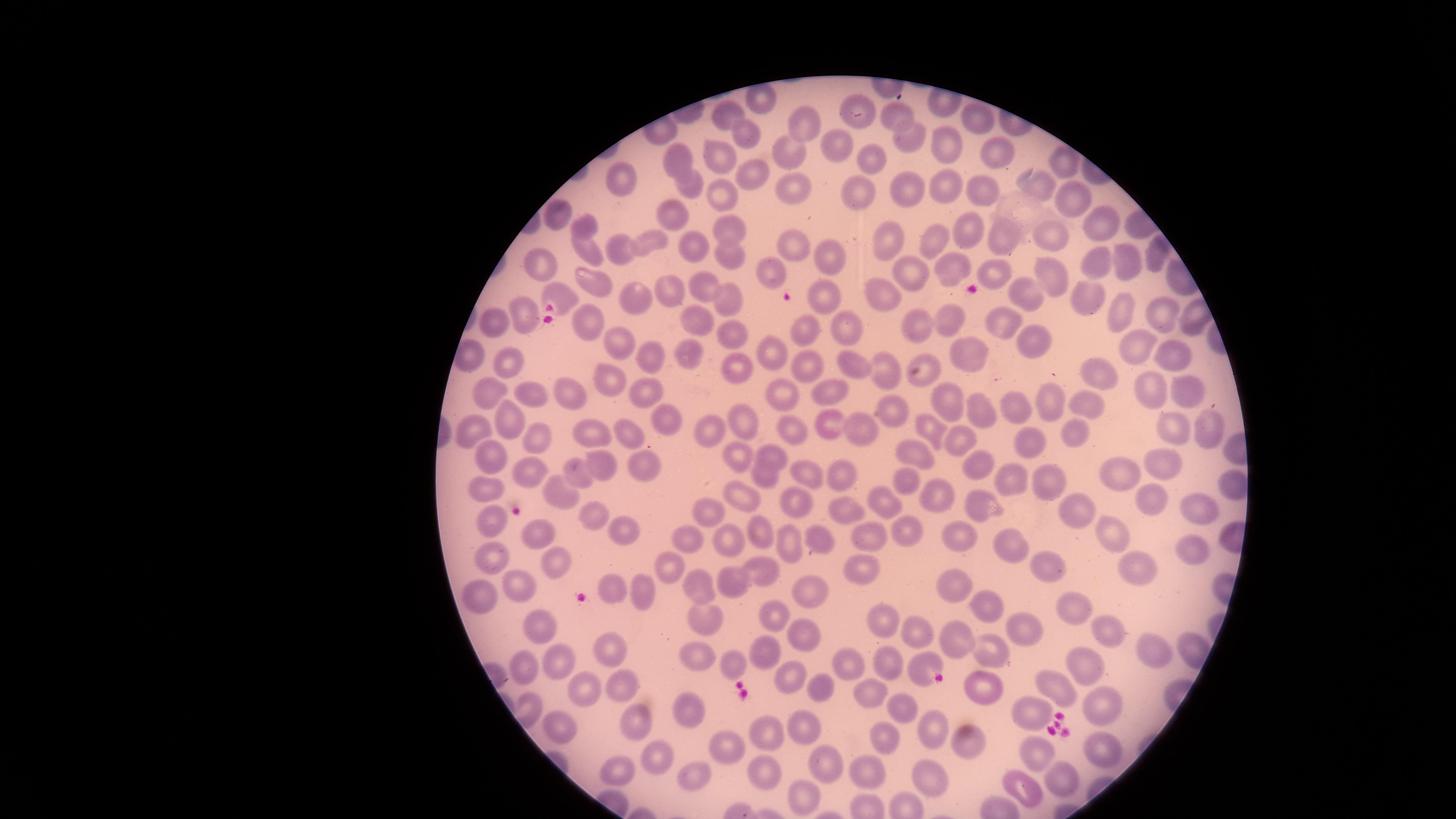

Approximate marker points, in pixels from the top-left corner. Uninfected red blood cells: (x=758, y=105), (x=858, y=106), (x=723, y=113), (x=896, y=117), (x=976, y=118), (x=800, y=123), (x=745, y=132), (x=909, y=141), (x=787, y=148), (x=840, y=149), (x=947, y=150), (x=673, y=152), (x=718, y=153), (x=991, y=153), (x=873, y=155), (x=1058, y=164), (x=619, y=177), (x=752, y=177), (x=687, y=183), (x=795, y=184), (x=949, y=187), (x=1039, y=187), (x=904, y=188), (x=717, y=190), (x=860, y=192), (x=985, y=193), (x=1070, y=201), (x=560, y=216), (x=673, y=217), (x=584, y=225), (x=1100, y=225), (x=724, y=226), (x=963, y=231), (x=1046, y=237), (x=647, y=241), (x=893, y=241), (x=933, y=241), (x=1004, y=241), (x=793, y=242), (x=583, y=244), (x=621, y=244), (x=693, y=248), (x=724, y=256), (x=833, y=258), (x=1094, y=259), (x=1122, y=260), (x=545, y=261), (x=953, y=267), (x=770, y=270), (x=998, y=273), (x=1047, y=273), (x=907, y=275), (x=704, y=283), (x=589, y=284), (x=555, y=290), (x=877, y=291), (x=669, y=292), (x=819, y=292), (x=1020, y=292), (x=627, y=293), (x=727, y=296), (x=1083, y=297), (x=522, y=312), (x=1160, y=312), (x=1116, y=314), (x=998, y=316), (x=948, y=321), (x=591, y=323), (x=695, y=323), (x=917, y=325), (x=490, y=326), (x=841, y=327), (x=803, y=329), (x=730, y=330), (x=620, y=341), (x=1034, y=342), (x=1129, y=342), (x=463, y=351), (x=1182, y=353), (x=684, y=354), (x=773, y=354), (x=964, y=354), (x=653, y=356), (x=850, y=359), (x=803, y=365), (x=512, y=366), (x=730, y=368), (x=1096, y=369), (x=885, y=372), (x=924, y=372), (x=610, y=378), (x=830, y=388), (x=647, y=389), (x=1182, y=389), (x=533, y=391), (x=1155, y=391), (x=497, y=392), (x=781, y=392), (x=572, y=395), (x=1049, y=400), (x=944, y=402), (x=1084, y=403), (x=889, y=407), (x=1020, y=407), (x=982, y=410), (x=514, y=417), (x=739, y=419), (x=670, y=420), (x=829, y=423), (x=1169, y=425), (x=1206, y=426), (x=864, y=428), (x=468, y=429), (x=626, y=429), (x=932, y=429), (x=715, y=432), (x=792, y=432), (x=586, y=433), (x=1068, y=433), (x=1026, y=438), (x=957, y=439), (x=536, y=441), (x=771, y=451), (x=912, y=453), (x=489, y=457), (x=739, y=457), (x=979, y=463), (x=648, y=464), (x=529, y=465), (x=604, y=465), (x=1156, y=465), (x=585, y=471), (x=838, y=471), (x=810, y=473), (x=1011, y=473), (x=1119, y=473), (x=764, y=477), (x=901, y=477), (x=1046, y=477), (x=1224, y=481), (x=564, y=491), (x=488, y=493), (x=744, y=494), (x=932, y=498), (x=1150, y=498), (x=798, y=503), (x=881, y=503), (x=970, y=505), (x=703, y=511), (x=843, y=511), (x=1193, y=511), (x=1080, y=512), (x=596, y=516), (x=493, y=517), (x=910, y=524), (x=626, y=528), (x=536, y=530), (x=768, y=530), (x=1108, y=530), (x=958, y=534), (x=863, y=535), (x=691, y=537), (x=795, y=538), (x=734, y=543), (x=815, y=543), (x=1007, y=546), (x=1190, y=554), (x=493, y=557), (x=757, y=565), (x=861, y=565), (x=673, y=567), (x=557, y=570), (x=1134, y=571), (x=1055, y=575), (x=738, y=579), (x=516, y=583), (x=695, y=583), (x=618, y=587), (x=960, y=587), (x=640, y=588), (x=807, y=588), (x=480, y=596), (x=985, y=606), (x=1083, y=609), (x=776, y=612), (x=880, y=615), (x=714, y=624), (x=545, y=628), (x=1028, y=630), (x=797, y=632), (x=909, y=632), (x=1114, y=632), (x=961, y=643), (x=1157, y=644), (x=611, y=645), (x=993, y=652), (x=698, y=655), (x=765, y=656), (x=557, y=663), (x=890, y=663), (x=921, y=664), (x=729, y=666), (x=527, y=667), (x=850, y=667), (x=1087, y=667), (x=790, y=675), (x=619, y=680), (x=1056, y=687), (x=586, y=689), (x=815, y=691), (x=984, y=691), (x=870, y=694), (x=1106, y=702), (x=896, y=706), (x=692, y=711), (x=1031, y=716), (x=638, y=719), (x=556, y=728), (x=807, y=729), (x=929, y=732), (x=886, y=735), (x=769, y=739), (x=968, y=743), (x=724, y=747), (x=1036, y=750), (x=1105, y=753), (x=655, y=763), (x=697, y=768), (x=868, y=769), (x=764, y=772), (x=827, y=773), (x=625, y=776), (x=938, y=777), (x=1066, y=779), (x=1020, y=792), (x=807, y=799). Single field of view. Thin smear of blood. Giemsa-stained preparation. Image is 1456×819 pixels. Presence: no malaria parasites identified. Smartphone photograph through the microscope eyepiece. Circular visible region.